Identify the preparation type.
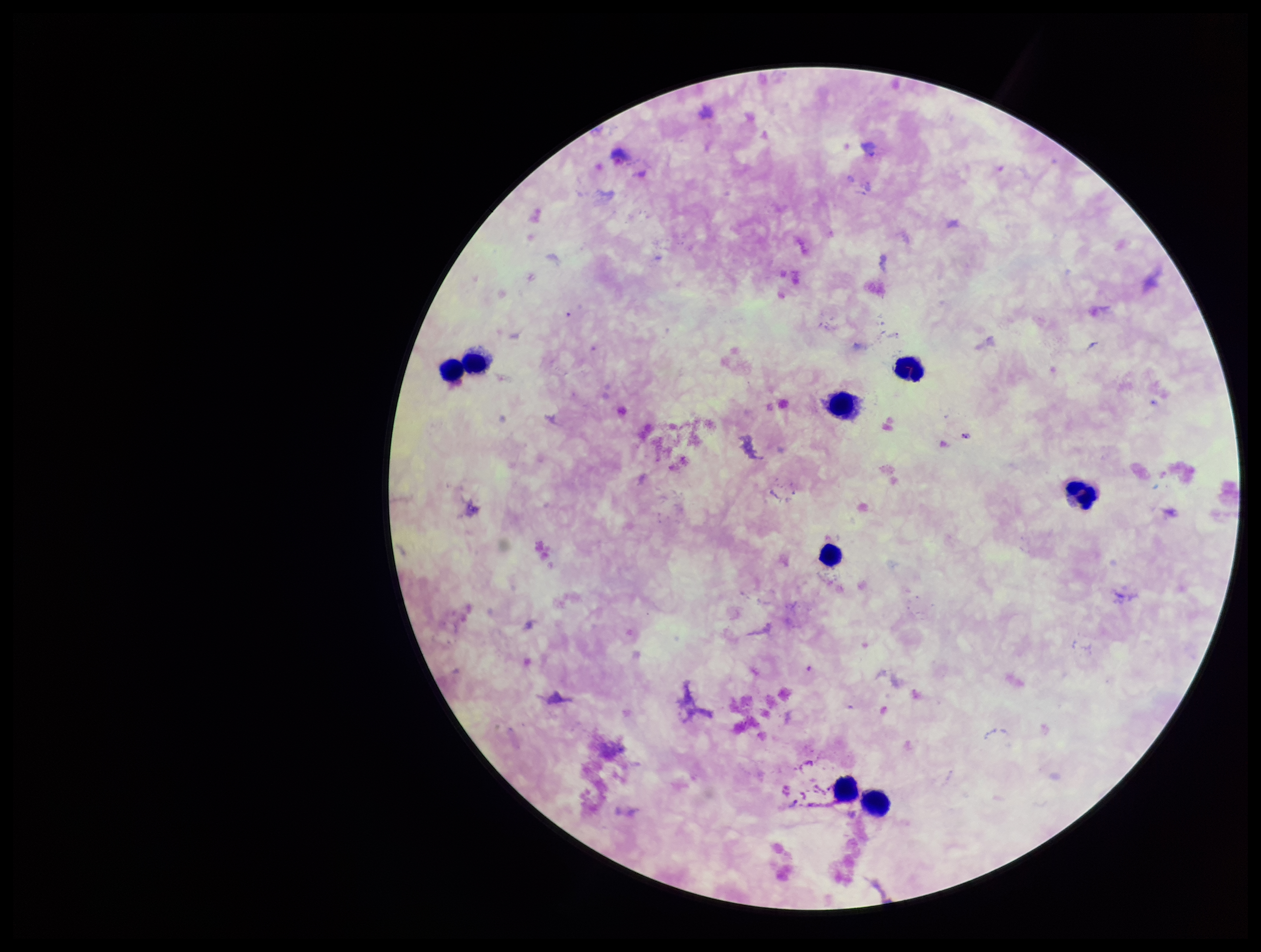

Thick.

Patient malaria status: infected. Leukocyte count: 8. Plasmodium parasites: detected. Smartphone photograph taken through the eyepiece of a microscope. Image is 1261×952 pixels. Parasite count: 1. Species reported for this patient: Plasmodium falciparum. Giemsa stain. One field from this slide.